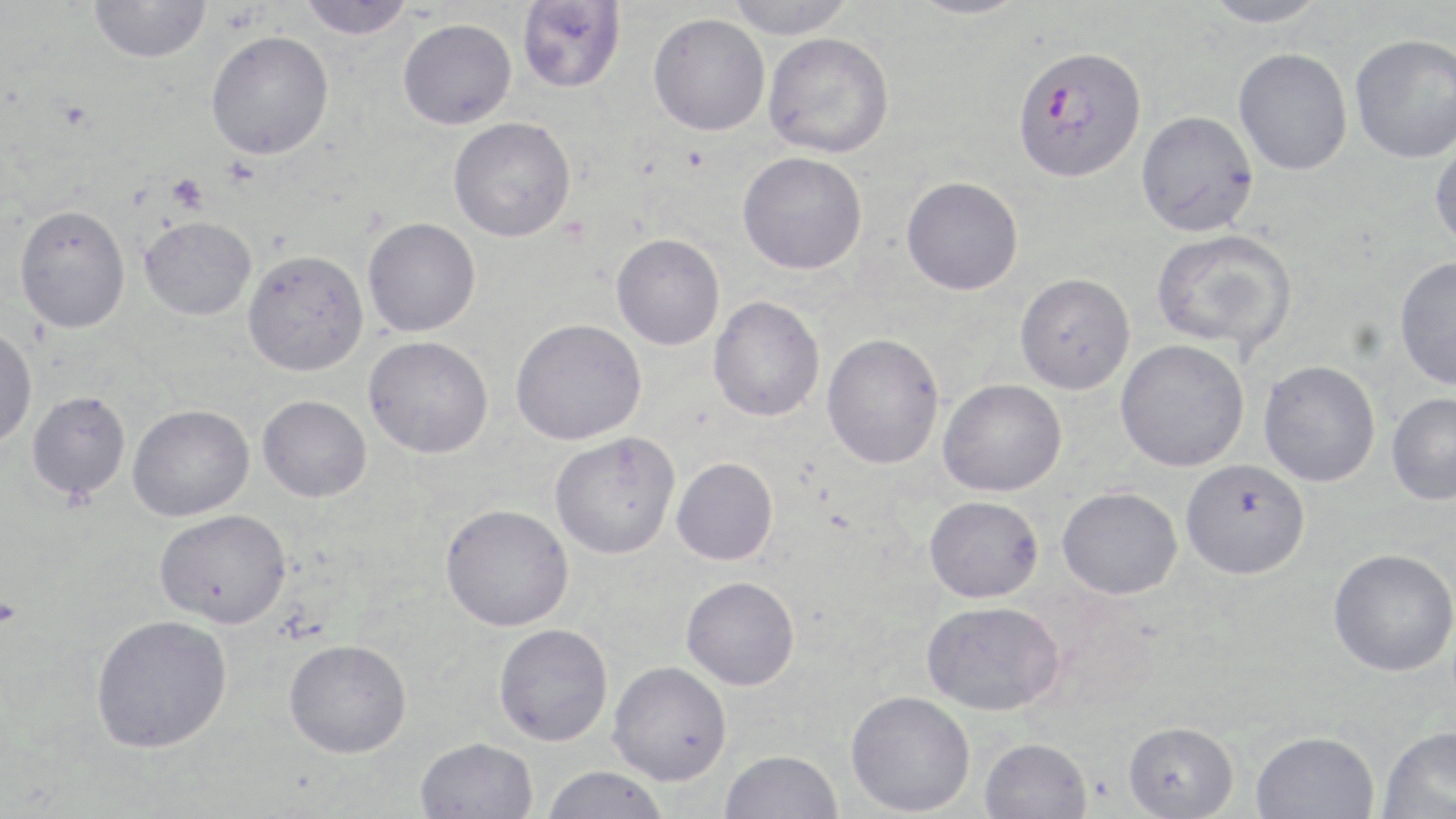

Summary:
  - Coordinate format: approximate bounding boxes as [x1, y1, x2, y2] in pixels
  - Plasmodium falciparum-infected red blood cell locations: [1013, 46, 1147, 182]
  - Uninfected red blood cell locations: [298, 0, 415, 40], [516, 0, 626, 93], [726, 0, 856, 39], [905, 0, 1033, 19], [1201, 0, 1331, 28], [88, 1, 212, 63], [648, 13, 769, 136], [398, 18, 517, 129], [205, 30, 334, 159], [763, 32, 895, 158], [1350, 33, 1456, 163], [1234, 48, 1352, 175], [1136, 110, 1258, 237], [448, 117, 576, 242], [1429, 134, 1456, 251], [737, 151, 867, 274], [901, 176, 1023, 295], [14, 204, 130, 333], [139, 216, 256, 320], [363, 217, 481, 337], [1151, 229, 1298, 356], [611, 233, 725, 350], [242, 249, 368, 375], [1394, 256, 1456, 390], [1015, 272, 1135, 394], [708, 296, 825, 422], [510, 318, 646, 445], [0, 327, 38, 447], [822, 332, 945, 469], [363, 335, 493, 458], [1115, 340, 1249, 472], [1258, 360, 1380, 487], [938, 379, 1067, 497], [27, 391, 131, 499], [1386, 393, 1456, 506], [258, 395, 372, 502], [127, 403, 254, 521], [549, 432, 680, 559], [671, 457, 778, 565], [1181, 459, 1311, 579], [1057, 486, 1182, 599], [924, 495, 1044, 602], [440, 503, 573, 631], [155, 508, 291, 628], [1328, 548, 1456, 676], [681, 576, 800, 690], [922, 600, 1064, 715], [89, 614, 232, 753], [493, 623, 613, 746], [284, 638, 412, 758], [608, 661, 731, 785], [845, 690, 975, 816], [1123, 721, 1239, 818], [1379, 724, 1456, 819], [1251, 730, 1379, 819], [415, 737, 538, 819], [979, 737, 1092, 819], [720, 749, 842, 819], [540, 765, 671, 819]
  - Platelet locations: [166, 173, 207, 213]
  - Slide-level diagnosis: Plasmodium falciparum
  - Modality: optical microscopy
  - Magnification: 1000x
  - Field of view: one of a larger specimen
  - Stain: May-Grünwald-Giemsa
  - Image size: 1456×819 pixels
  - Preparation: thin blood smear